Identify the parasite.
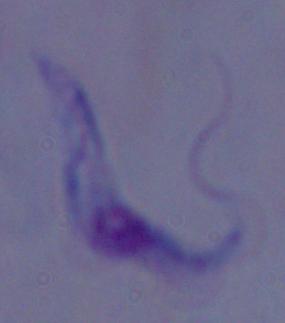

A trypanosome.

Summary:
  - Modality: photomicrograph
  - Magnification: 1000x